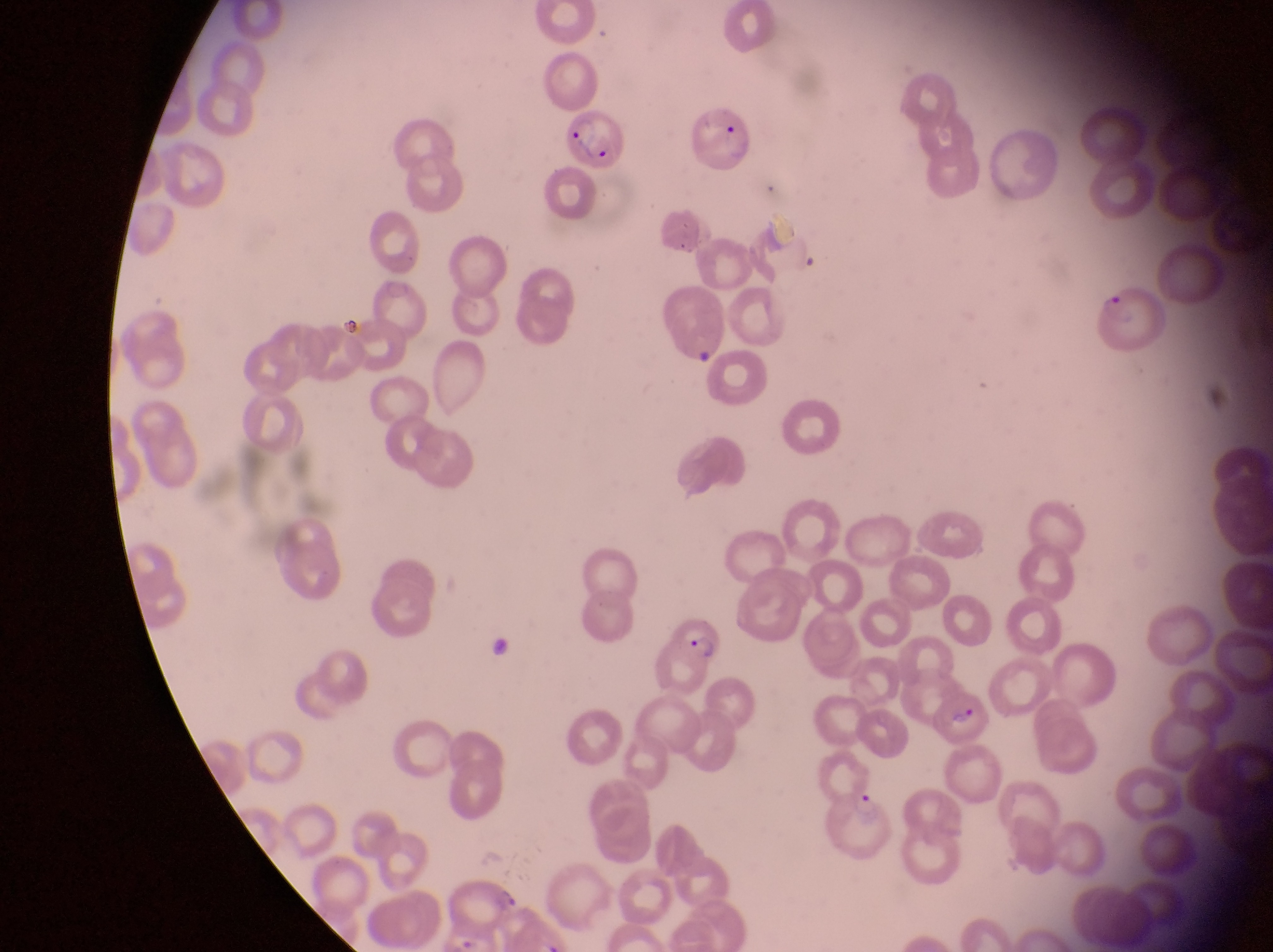
Approximate bounding boxes as (left, top, right, bottom) in pixels. Parasitised red blood cell locations: (687, 104, 764, 179), (564, 108, 631, 173), (1091, 278, 1169, 358), (657, 289, 727, 366), (667, 617, 725, 667), (928, 682, 993, 745), (829, 791, 898, 863). Collected in Uganda. Thin blood smear. Photographed through the eyepiece of an Olympus CX-23 microscope with a smartphone camera. Image is 1273×952 pixels. Magnification of 1000x. One field of view.